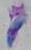
magnification = 1000x
modality = photomicrograph
identification = Toxoplasma gondii